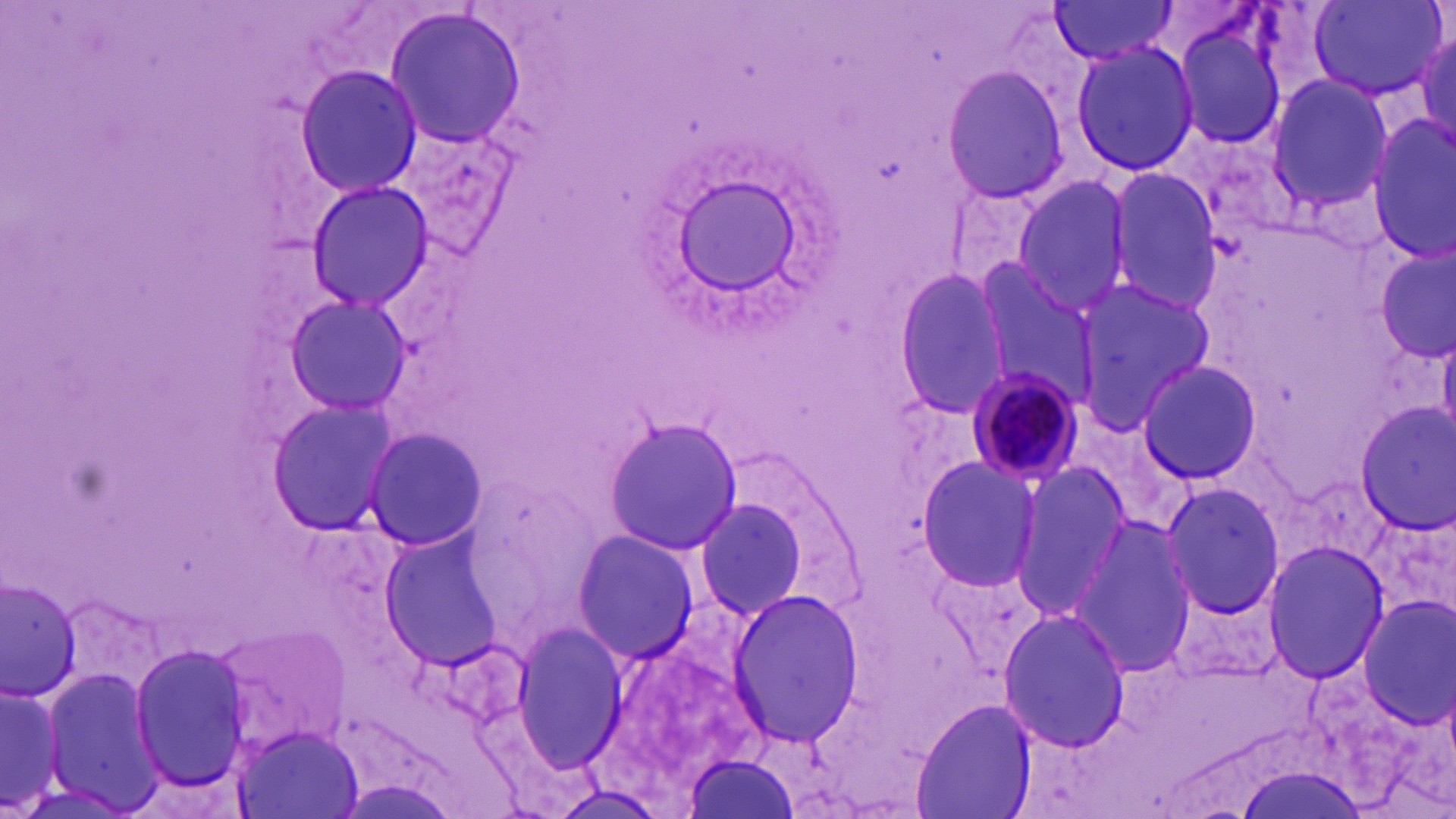

slide_level_diagnosis: Plasmodium malariae
field_of_view: one of a larger specimen
image_size: 1456×819 pixels
uninfected_red_blood_cell_locations: 'approximate bounding boxes as (x1,y1)-(x2,y2) corner pairs in pixels: (1307,0)-(1447,103), (1045,1)-(1181,64), (381,7)-(527,148), (1171,18)-(1289,153), (1410,27)-(1455,148), (1068,39)-(1202,178), (295,64)-(421,198), (939,64)-(1074,203), (1263,75)-(1394,210), (1368,117)-(1456,262), (387,120)-(525,261), (1102,167)-(1223,313), (667,174)-(810,304), (1007,174)-(1134,316), (303,180)-(436,313), (1373,246)-(1455,363), (971,262)-(1100,407), (893,272)-(1015,417), (1069,276)-(1214,429), (278,293)-(412,418), (1135,359)-(1265,486), (264,398)-(403,537), (1350,401)-(1456,534), (602,418)-(743,555), (360,426)-(488,553), (915,457)-(1045,590), (1010,463)-(1133,615), (1159,478)-(1286,619), (691,493)-(814,625), (1068,517)-(1200,678), (570,528)-(700,663), (380,530)-(509,667), (1263,541)-(1390,683), (1,577)-(81,698), (726,586)-(865,748), (1357,597)-(1456,730), (997,607)-(1132,754), (212,620)-(352,758), (512,620)-(628,772), (131,644)-(254,790), (39,666)-(163,815), (0,676)-(71,815), (911,699)-(1036,819), (230,722)-(367,818), (684,752)-(798,817)'
plasmodium_malariae_infected_red_blood_cell_locations: 'approximate bounding boxes as (x1,y1)-(x2,y2) corner pairs in pixels: (963,365)-(1087,489)'
preparation: thin blood smear
stain: May-Grünwald-Giemsa
magnification: 1000x
modality: optical microscopy